Point out each leukocyte.
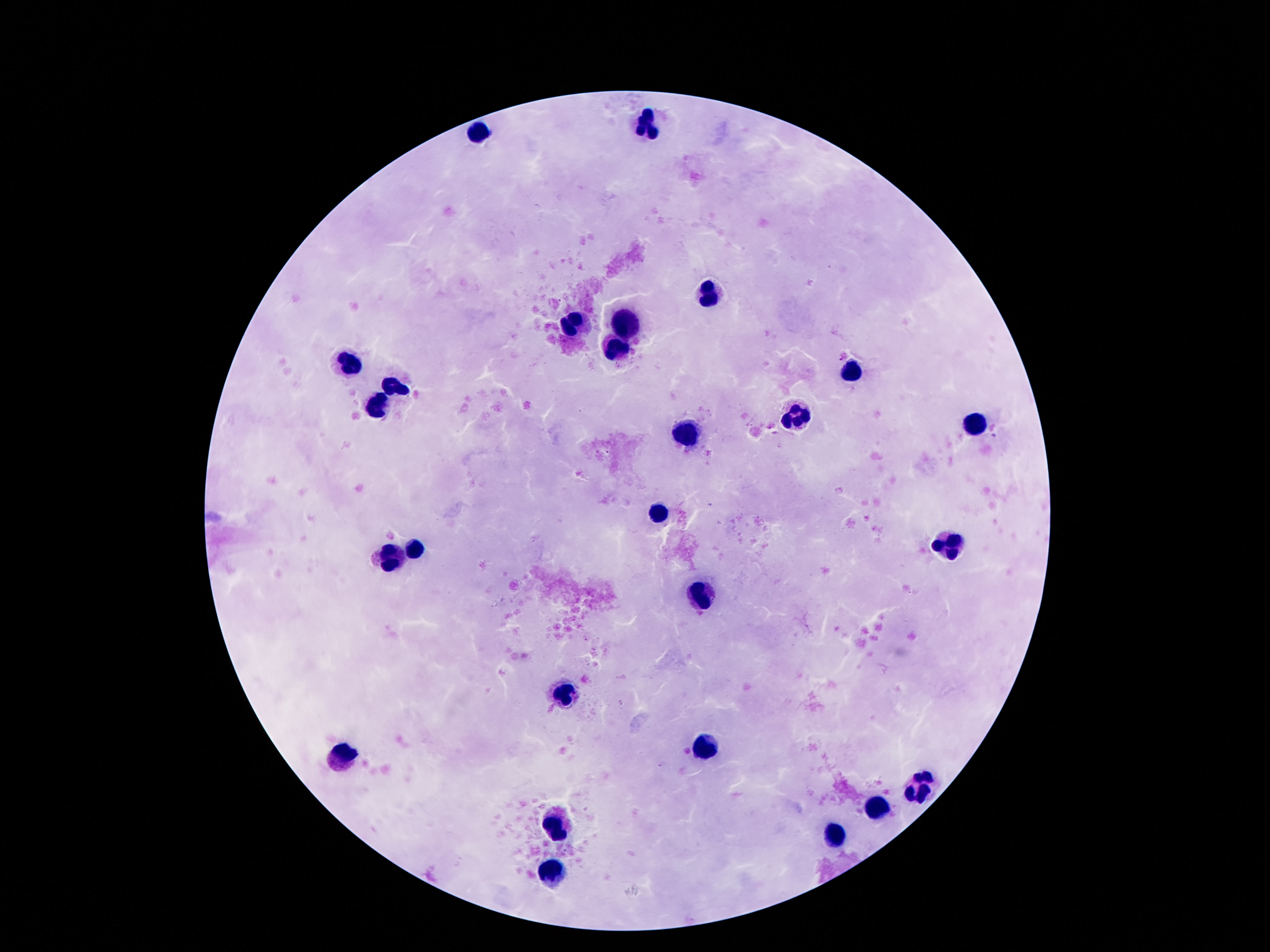

Approximate centers as (x, y) in pixels.
Leukocytes: (650, 123), (478, 130), (707, 293), (625, 321), (574, 325), (616, 347), (342, 360), (856, 373), (394, 386), (375, 408), (795, 414), (975, 424), (692, 436), (658, 510), (954, 543), (413, 545), (394, 556), (702, 599), (566, 696), (705, 746), (344, 756), (917, 787), (877, 809), (556, 823), (835, 835), (551, 874).

Giemsa stain. Image is 1270×952 pixels. 100x magnification. Thick peripheral-blood smear. Photographed through the microscope eyepiece with a smartphone camera. Single field of view. Patient malaria status: not infected.